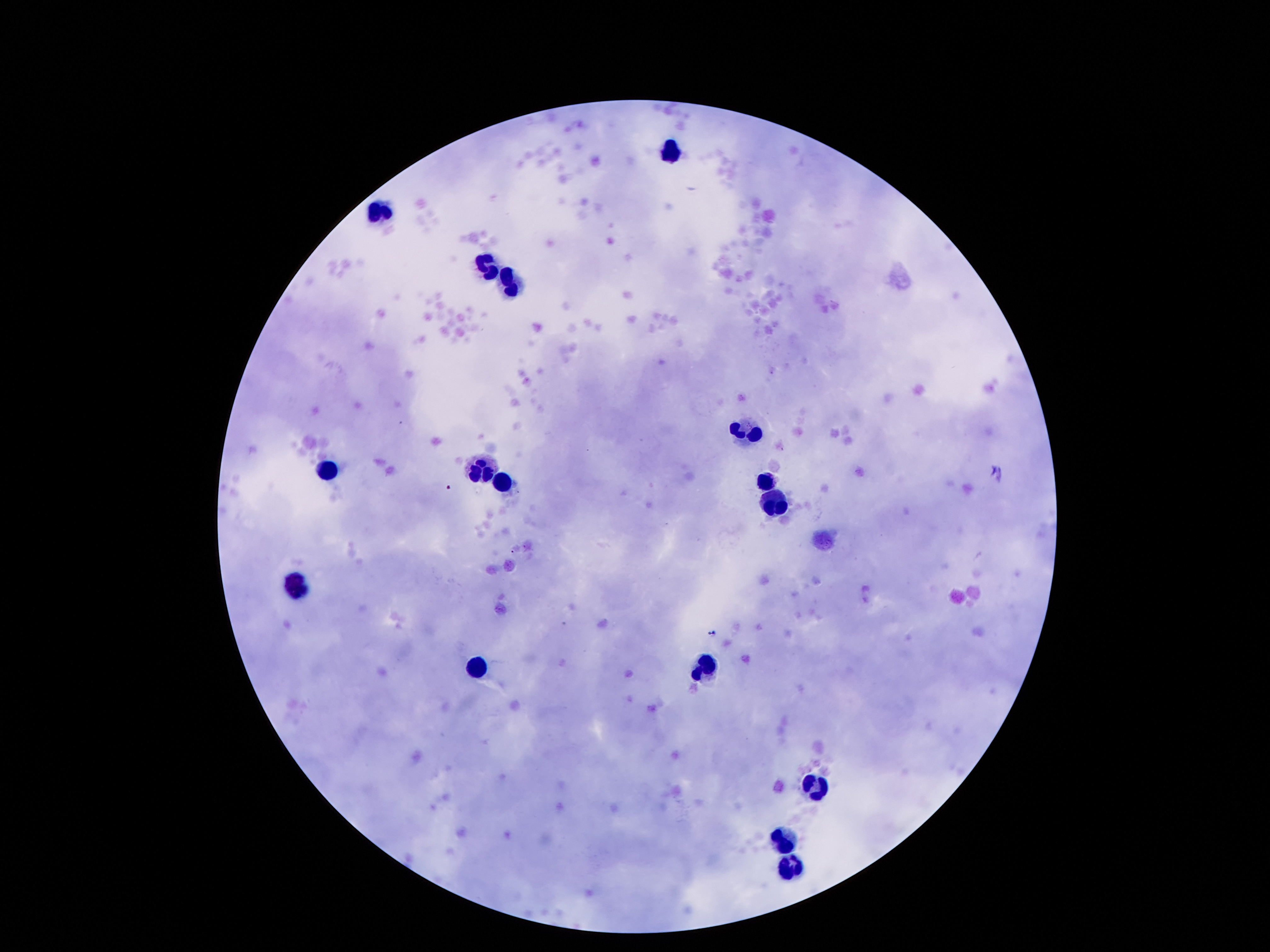
Approximate centers as {x, y} in pixels.
Summary:
  - Leukocyte locations: {671, 152}, {377, 210}, {480, 266}, {510, 282}, {748, 429}, {480, 467}, {326, 471}, {767, 481}, {503, 485}, {779, 502}, {296, 588}, {704, 667}, {480, 672}, {818, 786}, {786, 840}, {790, 868}
  - Magnification: 100x
  - Stain: Giemsa
  - Field of view: one from this slide
  - Preparation: thick blood film
  - Capture: smartphone camera through the microscope eyepiece
  - Patient malaria status: uninfected
  - Image size: 1270×952 pixels